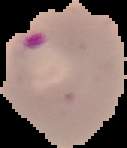 Cell region segmented out of the field of view; the surrounding area is masked to black. Image is 127×148 pixels. Malaria status: parasitized. From a thin blood smear.